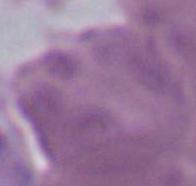

Summary:
  - Magnification: 1000x
  - Identification: erythrocyte
  - Modality: micrograph